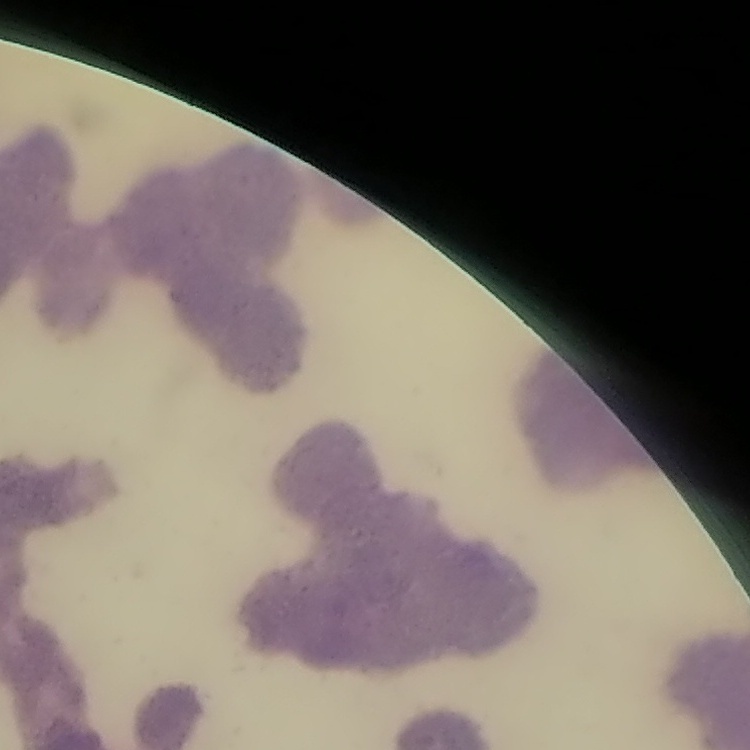

Summary:
  - Erythrocyte morphology: rouleaux formation
  - Image type: one tile cut from a larger photomicrograph
  - Preparation: thin blood film
  - Stain: Field's or Giemsa